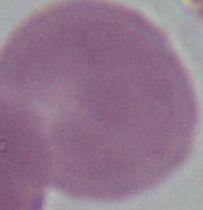

magnification: 1000x
identification: erythrocyte
modality: micrograph